Comment on the morphology of the red blood cells.
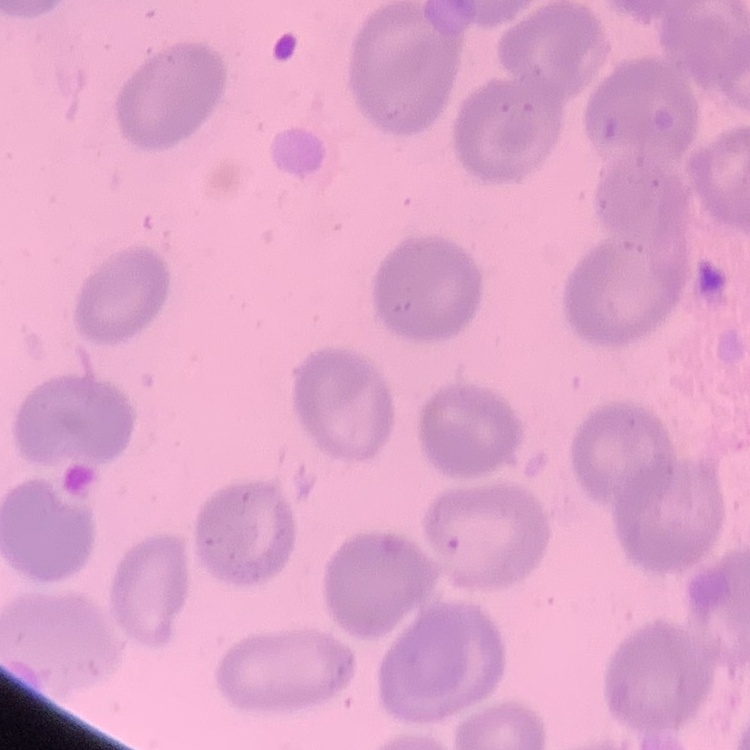

They show no rouleaux formation.

Summary:
  - Image type: square crop of a larger photomicrograph
  - Stain: Field's or Giemsa
  - Preparation: thin peripheral smear